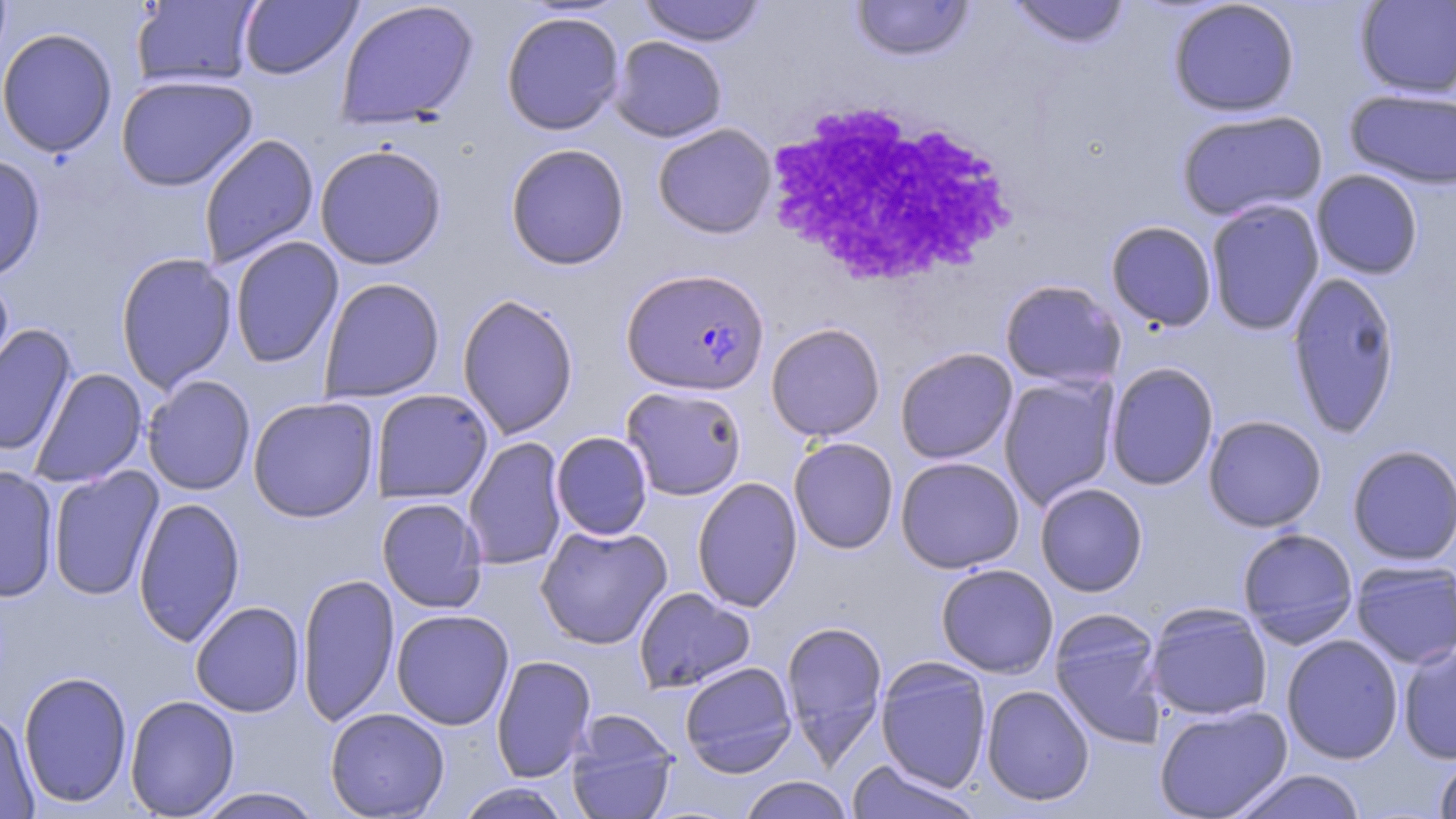
Summary:
  - Coordinate format: approximate bounding boxes as [x1, y1, x2, y2] in pixels
  - Uninfected red blood cell locations: [131, 0, 263, 88], [238, 0, 361, 80], [638, 0, 767, 47], [849, 0, 976, 62], [1008, 0, 1131, 49], [1167, 0, 1301, 117], [1354, 0, 1456, 99], [336, 1, 479, 129], [500, 10, 626, 136], [0, 28, 118, 158], [609, 36, 727, 142], [115, 74, 258, 191], [1344, 88, 1456, 189], [1176, 109, 1328, 222], [652, 123, 777, 239], [198, 133, 319, 269], [314, 143, 448, 270], [505, 143, 630, 270], [0, 153, 46, 281], [1311, 169, 1423, 279], [1205, 199, 1325, 336], [1105, 220, 1218, 331], [229, 236, 344, 369], [116, 253, 238, 392], [0, 271, 15, 394], [1286, 271, 1401, 438], [319, 277, 445, 403], [999, 279, 1125, 390], [457, 293, 579, 440], [765, 322, 886, 441], [0, 324, 77, 457], [895, 347, 1018, 464], [1105, 362, 1219, 490], [29, 367, 147, 487], [141, 375, 256, 496], [998, 375, 1119, 510], [620, 385, 747, 501], [370, 389, 494, 505], [246, 396, 380, 523], [1203, 415, 1327, 532], [550, 431, 653, 540], [462, 436, 568, 571], [788, 437, 899, 554], [1347, 444, 1456, 566], [895, 456, 1024, 573], [0, 465, 59, 602], [47, 466, 164, 601], [692, 476, 802, 612], [1034, 482, 1148, 596], [133, 496, 245, 647], [376, 497, 488, 613], [535, 523, 672, 650], [1237, 527, 1359, 647], [1350, 559, 1455, 668], [935, 563, 1059, 678], [296, 572, 400, 728], [633, 587, 755, 694], [190, 601, 306, 717], [1145, 603, 1273, 721], [1048, 608, 1167, 749], [391, 609, 514, 730], [780, 619, 889, 766], [1281, 634, 1404, 764], [1397, 643, 1456, 764], [491, 655, 597, 782], [876, 658, 992, 792], [679, 661, 797, 777], [18, 670, 133, 808], [981, 685, 1095, 806], [125, 695, 240, 817], [1154, 703, 1293, 818], [324, 707, 450, 818], [0, 710, 40, 819], [565, 713, 679, 819], [1433, 753, 1456, 818], [844, 760, 985, 819], [1228, 768, 1367, 819], [737, 776, 856, 818], [454, 782, 574, 819], [192, 787, 326, 818]
  - Plasmodium falciparum-infected red blood cell locations: [621, 267, 769, 395]
  - White blood cell locations: [762, 99, 1016, 289]
  - Slide-level diagnosis: Plasmodium falciparum
  - Stain: May-Grünwald-Giemsa
  - Field of view: single
  - Image size: 1456×819 pixels
  - Magnification: 1000x
  - Modality: optical microscopy
  - Preparation: thin blood film